Name the parasite shown.
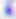
Toxoplasma gondii.

Captured at 400x magnification. Photomicrograph.